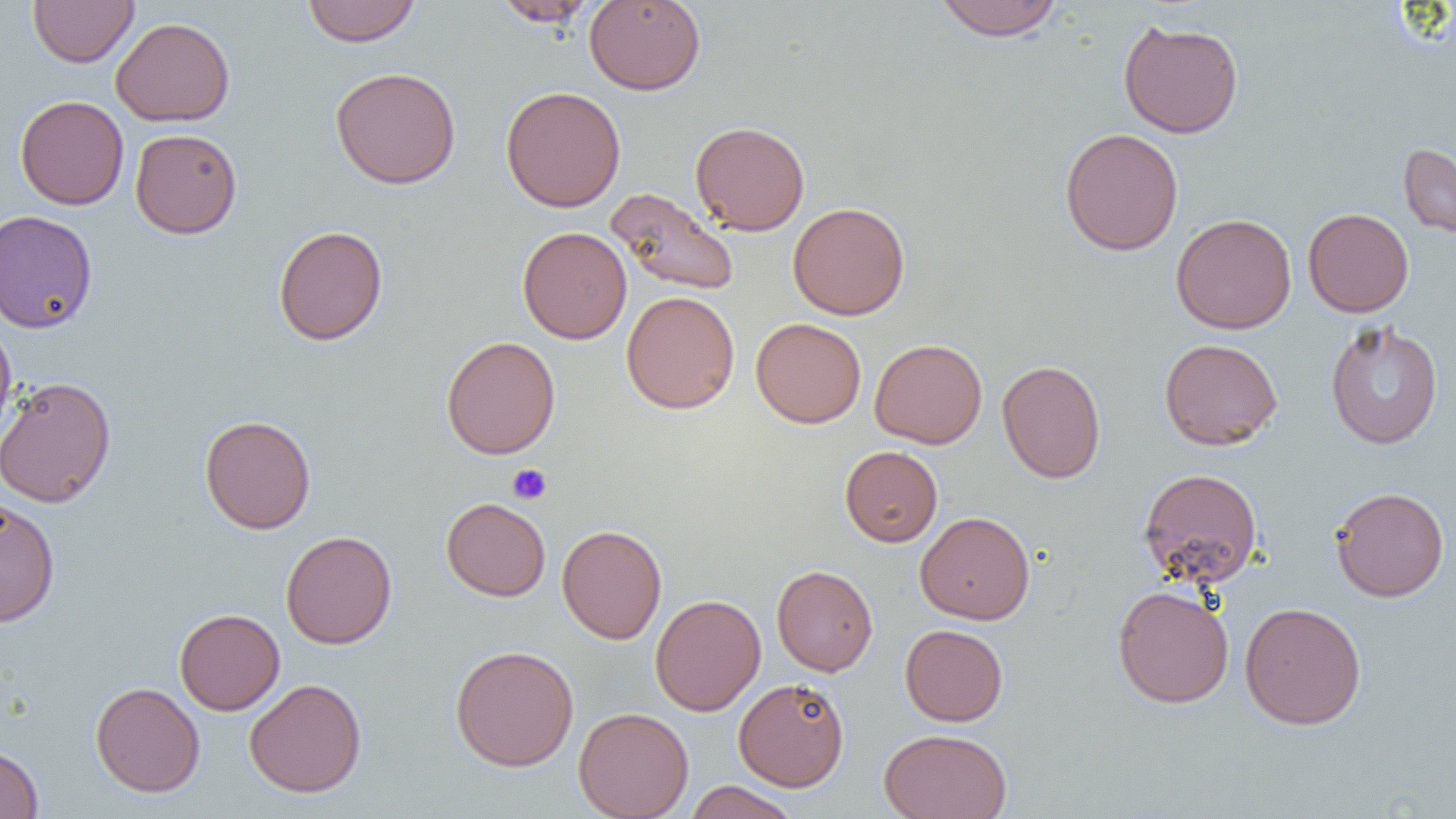

Summary:
  - Coordinate format: approximate bounding boxes as named x1/y1/x2/y2 corners in pixels
  - Uninfected red blood cell locations: (x1=28, y1=0, x2=139, y2=67), (x1=303, y1=0, x2=420, y2=47), (x1=491, y1=0, x2=599, y2=27), (x1=584, y1=0, x2=706, y2=95), (x1=934, y1=0, x2=1065, y2=41), (x1=110, y1=16, x2=235, y2=126), (x1=1118, y1=17, x2=1244, y2=138), (x1=330, y1=67, x2=461, y2=189), (x1=501, y1=85, x2=626, y2=212), (x1=15, y1=95, x2=129, y2=209), (x1=690, y1=120, x2=810, y2=235), (x1=130, y1=128, x2=242, y2=238), (x1=1059, y1=128, x2=1183, y2=256), (x1=1398, y1=142, x2=1456, y2=240), (x1=606, y1=188, x2=739, y2=297), (x1=787, y1=202, x2=910, y2=320), (x1=1303, y1=208, x2=1414, y2=317), (x1=0, y1=210, x2=98, y2=334), (x1=1170, y1=213, x2=1297, y2=334), (x1=273, y1=225, x2=388, y2=346), (x1=517, y1=226, x2=632, y2=344), (x1=621, y1=291, x2=740, y2=414), (x1=751, y1=318, x2=866, y2=428), (x1=1324, y1=321, x2=1443, y2=449), (x1=0, y1=322, x2=17, y2=444), (x1=441, y1=335, x2=560, y2=460), (x1=869, y1=338, x2=987, y2=449), (x1=1159, y1=338, x2=1283, y2=450), (x1=997, y1=359, x2=1106, y2=484), (x1=0, y1=376, x2=116, y2=508), (x1=199, y1=414, x2=316, y2=534), (x1=840, y1=445, x2=942, y2=547), (x1=1138, y1=467, x2=1263, y2=588), (x1=1330, y1=486, x2=1450, y2=602), (x1=441, y1=497, x2=551, y2=601), (x1=0, y1=498, x2=60, y2=627), (x1=915, y1=511, x2=1035, y2=625), (x1=557, y1=524, x2=667, y2=644), (x1=280, y1=531, x2=397, y2=649), (x1=771, y1=565, x2=878, y2=676), (x1=1112, y1=585, x2=1234, y2=708), (x1=650, y1=594, x2=766, y2=716), (x1=1239, y1=601, x2=1367, y2=730), (x1=174, y1=608, x2=285, y2=715), (x1=900, y1=624, x2=1009, y2=726), (x1=450, y1=644, x2=579, y2=771), (x1=733, y1=677, x2=850, y2=791), (x1=244, y1=678, x2=367, y2=797), (x1=90, y1=681, x2=205, y2=797), (x1=573, y1=707, x2=693, y2=818), (x1=879, y1=728, x2=1011, y2=818), (x1=0, y1=743, x2=44, y2=819), (x1=684, y1=781, x2=800, y2=819)
  - Platelet locations: (x1=507, y1=463, x2=552, y2=505)
  - Slide-level diagnosis: negative for blood parasites
  - Magnification: 1000x
  - Image size: 1456×819 pixels
  - Modality: light microscopy
  - Preparation: thin blood film
  - Field of view: single